Report the malaria status of this cell.
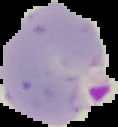

Parasitized.

Cell region segmented out of the field of view; the surrounding area is masked to black. Image is 118×127 pixels. From a thin blood film.